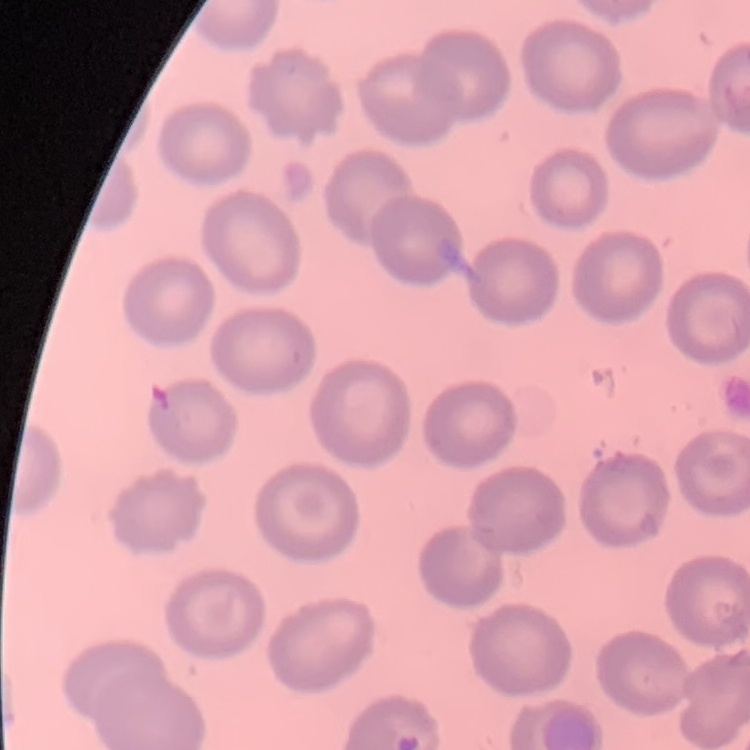
erythrocyte_morphology: no rouleaux formation
image_type: square crop of a larger photomicrograph
preparation: thin peripheral smear
stain: Field's or Giemsa